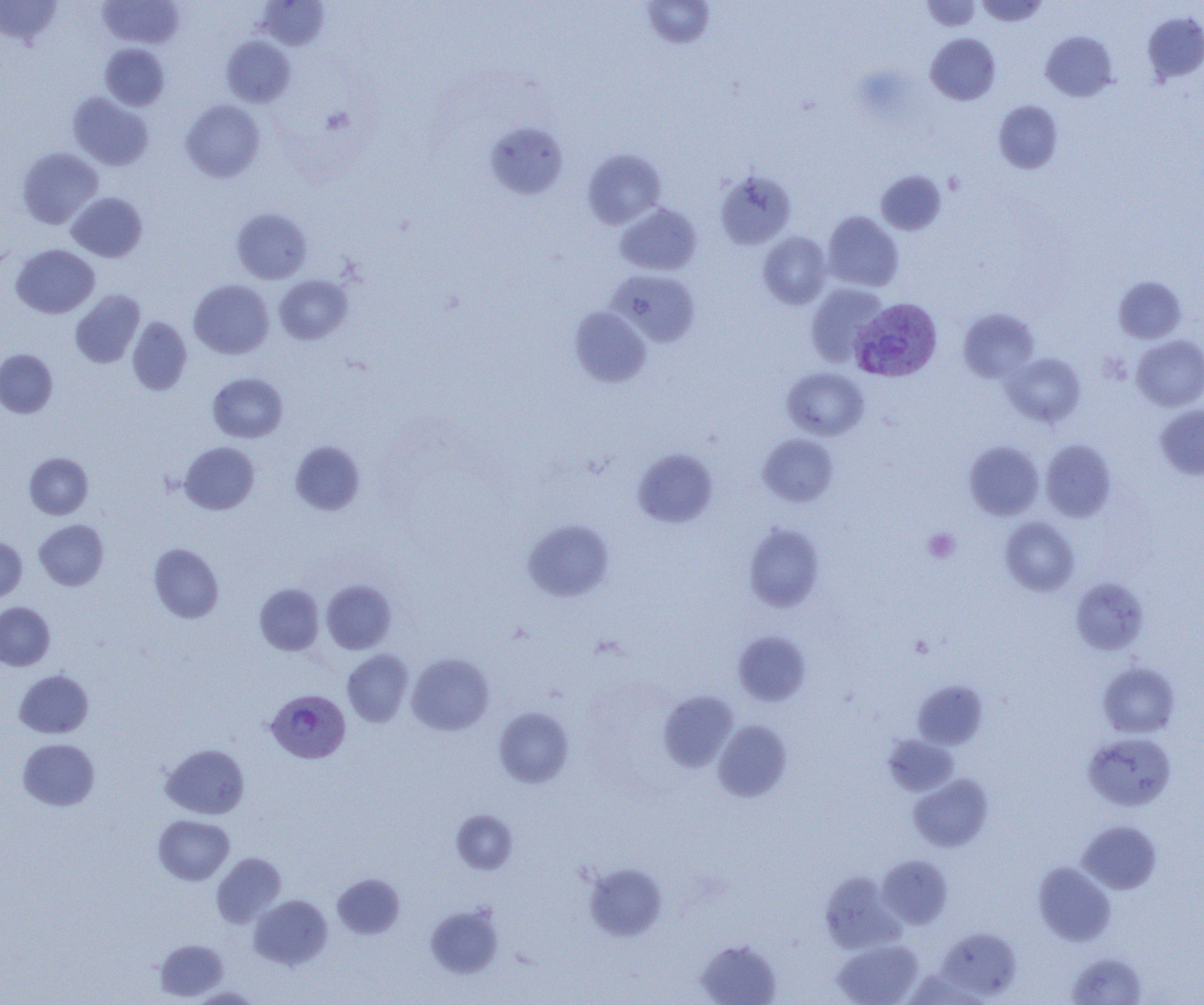 Approximate bounding boxes as (x1, y1, x2, y2) in pixels. Uninfected red blood cell locations: (0, 0, 62, 47), (98, 0, 184, 49), (641, 0, 716, 49), (921, 0, 981, 31), (976, 0, 1048, 26), (257, 1, 330, 49), (1142, 12, 1204, 84), (1041, 31, 1117, 101), (925, 33, 1000, 105), (221, 36, 296, 108), (100, 44, 170, 110), (68, 92, 154, 171), (181, 99, 265, 182), (993, 100, 1063, 173), (485, 122, 568, 199), (17, 147, 103, 229), (582, 148, 666, 229), (715, 169, 796, 249), (876, 170, 946, 235), (67, 192, 148, 262), (615, 203, 702, 275), (231, 207, 312, 284), (823, 211, 904, 292), (758, 231, 832, 309), (11, 244, 99, 318), (608, 269, 700, 347), (274, 274, 352, 345), (1113, 276, 1186, 344), (189, 279, 274, 359), (806, 283, 887, 367), (70, 290, 145, 368), (569, 306, 651, 387), (958, 308, 1039, 382), (127, 317, 192, 395), (1132, 335, 1204, 411), (0, 349, 58, 418), (1002, 352, 1086, 427), (782, 367, 869, 441), (208, 372, 288, 443), (1155, 405, 1204, 479), (758, 434, 839, 506), (1041, 439, 1116, 521), (290, 440, 365, 514), (179, 441, 260, 514), (964, 441, 1044, 520), (632, 448, 718, 528), (24, 452, 93, 519), (1000, 517, 1079, 596), (34, 519, 108, 590), (523, 519, 614, 601), (743, 523, 824, 612), (0, 537, 27, 602), (148, 543, 224, 623), (1070, 578, 1149, 655), (322, 580, 396, 654), (254, 583, 324, 656), (0, 601, 55, 670), (733, 631, 811, 706), (342, 649, 413, 727), (407, 653, 494, 736), (1097, 661, 1180, 738), (14, 669, 93, 738), (912, 680, 988, 750), (659, 691, 738, 771), (494, 707, 574, 788), (713, 720, 792, 802), (1083, 732, 1176, 811), (883, 734, 959, 796), (18, 739, 99, 811), (160, 743, 250, 819), (908, 774, 993, 852), (452, 810, 517, 873), (153, 815, 234, 885), (1077, 820, 1161, 894), (211, 852, 286, 927), (877, 855, 953, 928), (584, 862, 667, 941), (1033, 862, 1116, 946), (820, 871, 902, 952), (332, 874, 404, 939), (248, 894, 333, 970), (426, 905, 503, 978), (936, 927, 1022, 1000), (695, 938, 782, 1005), (155, 939, 227, 1000), (833, 939, 923, 1005), (1066, 952, 1149, 1005), (189, 986, 261, 1004). Plasmodium vivax-infected red blood cell locations: (851, 297, 943, 383), (266, 689, 350, 763). Platelet locations: (923, 529, 960, 563). Slide-level diagnosis: Plasmodium vivax. Thin blood film. Single field of view. Optical microscopy. 1000x magnification. Image is 1204×1005 pixels.